Describe the morphology of the red blood cells.
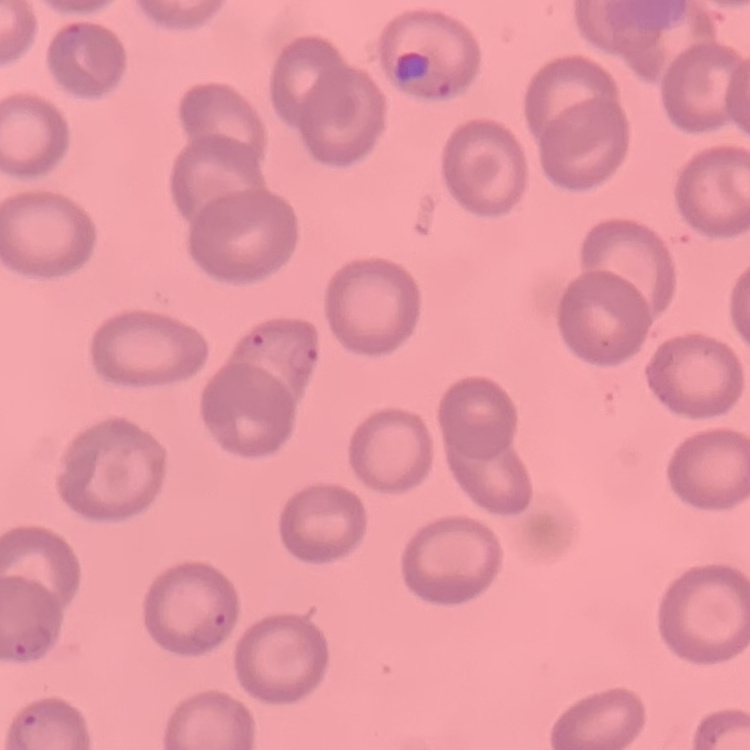
No rouleaux formation.

Field's or Giemsa stain. Thin peripheral smear. One tile cut from a larger photomicrograph.